Assess for malaria.
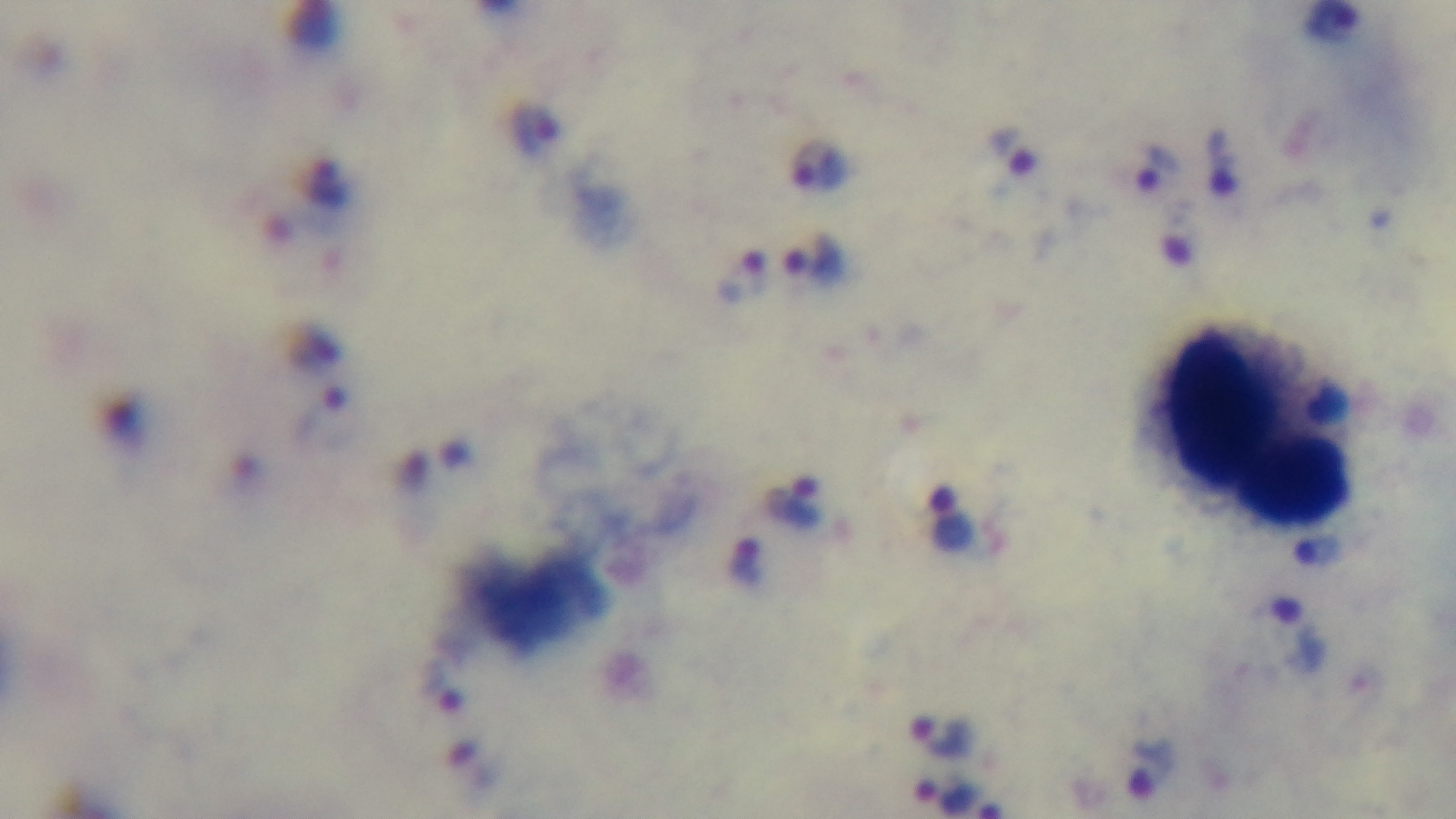
It is infected.

{
  "stain": "Giemsa",
  "objective": "100x oil immersion",
  "modality": "light microscopy",
  "preparation": "thick smear",
  "field_of_view": "single",
  "capture": "mounted 4K digital camera"
}